Comment on the morphology of the red blood cells.
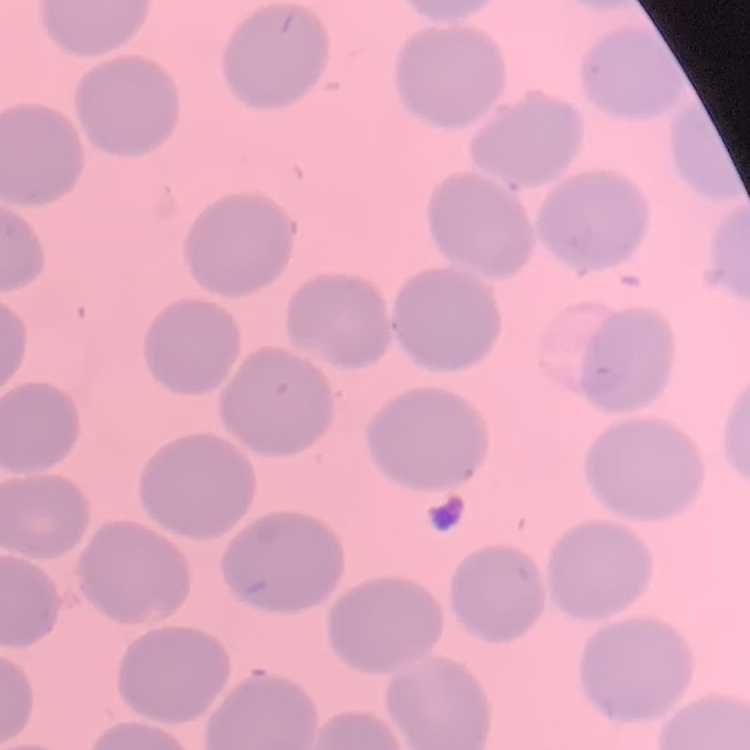

No rouleaux formation.

Summary:
  - Image type: one tile cut from a larger photomicrograph
  - Preparation: thin blood smear
  - Stain: Field's or Giemsa